Locate every malaria parasite.
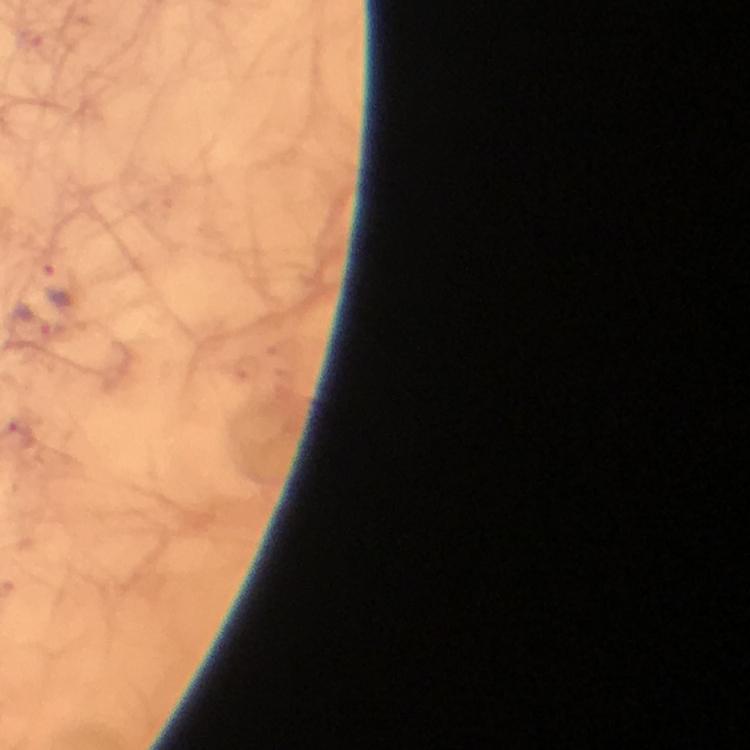
Approximate centers as [x, y] in pixels.
Malaria parasites: [61, 284], [30, 324].

Summary:
  - Image size: 750×750 pixels
  - Context: from a malaria diagnostic workup
  - Cropped from: a single field of view
  - Capture: smartphone camera through the microscope
  - Preparation: thick smear
  - Magnification: 100x
  - Immersion oil: applied
  - Stain: Giemsa